Locate every Plasmodium falciparum-infected red blood cell.
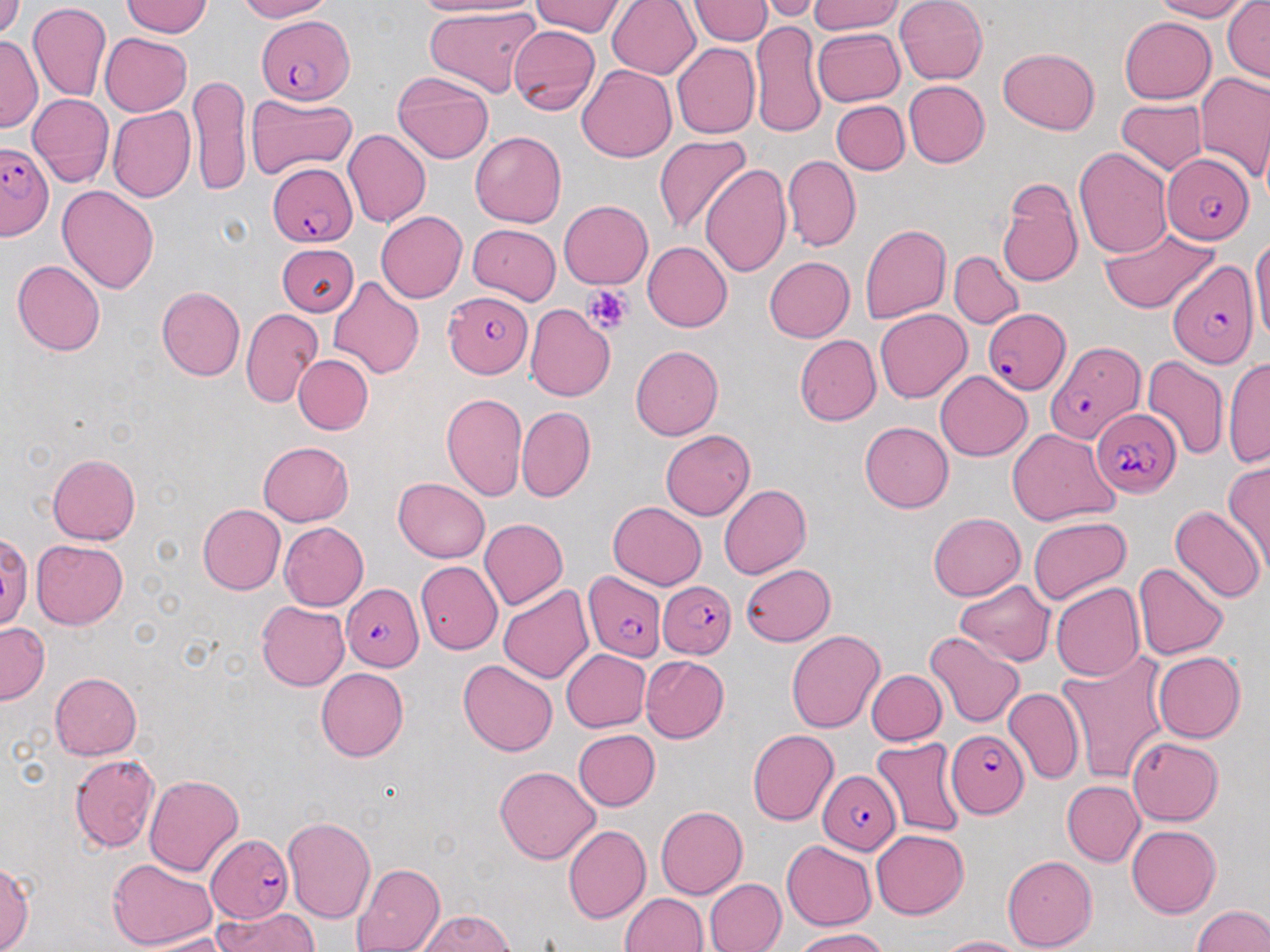

Approximate bounding boxes as named x1/y1/x2/y2 corners in pixels.
Plasmodium falciparum-infected red blood cells: (x1=258, y1=13, x2=354, y2=103), (x1=0, y1=142, x2=54, y2=241), (x1=1162, y1=152, x2=1254, y2=244), (x1=266, y1=162, x2=356, y2=247), (x1=1168, y1=257, x2=1259, y2=366), (x1=443, y1=291, x2=532, y2=377), (x1=982, y1=308, x2=1070, y2=394), (x1=1042, y1=340, x2=1145, y2=447), (x1=1091, y1=408, x2=1182, y2=497), (x1=583, y1=572, x2=666, y2=660), (x1=658, y1=582, x2=736, y2=659), (x1=339, y1=583, x2=424, y2=670), (x1=948, y1=727, x2=1029, y2=817), (x1=816, y1=770, x2=901, y2=853), (x1=206, y1=834, x2=293, y2=922).

Platelet locations: (x1=584, y1=285, x2=631, y2=333). Uninfected red blood cell locations: (x1=0, y1=0, x2=26, y2=40), (x1=236, y1=0, x2=332, y2=22), (x1=411, y1=0, x2=533, y2=18), (x1=689, y1=0, x2=774, y2=44), (x1=811, y1=0, x2=902, y2=35), (x1=894, y1=0, x2=987, y2=85), (x1=1149, y1=0, x2=1252, y2=21), (x1=1222, y1=0, x2=1269, y2=81), (x1=121, y1=1, x2=213, y2=36), (x1=529, y1=1, x2=626, y2=37), (x1=607, y1=1, x2=700, y2=79), (x1=757, y1=1, x2=825, y2=22), (x1=27, y1=3, x2=112, y2=102), (x1=422, y1=5, x2=545, y2=99), (x1=1119, y1=16, x2=1216, y2=103), (x1=749, y1=19, x2=826, y2=140), (x1=508, y1=24, x2=599, y2=113), (x1=813, y1=28, x2=904, y2=106), (x1=100, y1=32, x2=192, y2=116), (x1=0, y1=35, x2=42, y2=132), (x1=672, y1=42, x2=761, y2=139), (x1=997, y1=47, x2=1100, y2=135), (x1=578, y1=65, x2=677, y2=163), (x1=392, y1=70, x2=493, y2=163), (x1=1194, y1=70, x2=1270, y2=182), (x1=190, y1=74, x2=250, y2=195), (x1=904, y1=80, x2=990, y2=167), (x1=247, y1=92, x2=356, y2=181), (x1=27, y1=93, x2=114, y2=188), (x1=1116, y1=100, x2=1208, y2=174), (x1=831, y1=101, x2=910, y2=175), (x1=107, y1=107, x2=196, y2=203), (x1=342, y1=130, x2=431, y2=228), (x1=470, y1=131, x2=566, y2=227), (x1=654, y1=135, x2=750, y2=236), (x1=1073, y1=148, x2=1172, y2=257), (x1=782, y1=155, x2=861, y2=251), (x1=700, y1=164, x2=791, y2=277), (x1=997, y1=178, x2=1083, y2=287), (x1=57, y1=185, x2=160, y2=294), (x1=559, y1=200, x2=653, y2=289), (x1=375, y1=211, x2=468, y2=303), (x1=468, y1=224, x2=560, y2=302), (x1=859, y1=224, x2=951, y2=324), (x1=1101, y1=225, x2=1220, y2=313), (x1=1250, y1=229, x2=1270, y2=350), (x1=642, y1=241, x2=732, y2=331), (x1=278, y1=244, x2=358, y2=316), (x1=949, y1=251, x2=1023, y2=329), (x1=764, y1=256, x2=855, y2=342), (x1=13, y1=259, x2=105, y2=356), (x1=328, y1=276, x2=425, y2=378), (x1=156, y1=286, x2=245, y2=380), (x1=524, y1=304, x2=616, y2=401), (x1=241, y1=308, x2=322, y2=408), (x1=875, y1=308, x2=971, y2=403), (x1=794, y1=335, x2=881, y2=426), (x1=630, y1=345, x2=724, y2=440), (x1=294, y1=354, x2=373, y2=435), (x1=1223, y1=354, x2=1269, y2=468), (x1=1142, y1=355, x2=1229, y2=462), (x1=934, y1=369, x2=1032, y2=461), (x1=440, y1=393, x2=527, y2=501), (x1=517, y1=406, x2=596, y2=502), (x1=859, y1=421, x2=954, y2=512), (x1=1007, y1=427, x2=1119, y2=525), (x1=659, y1=429, x2=756, y2=520), (x1=257, y1=441, x2=354, y2=526), (x1=47, y1=453, x2=141, y2=544), (x1=1223, y1=461, x2=1270, y2=573), (x1=393, y1=477, x2=490, y2=563), (x1=719, y1=484, x2=811, y2=579), (x1=607, y1=502, x2=707, y2=589), (x1=197, y1=504, x2=286, y2=595), (x1=1170, y1=505, x2=1264, y2=603), (x1=928, y1=511, x2=1026, y2=600), (x1=1028, y1=517, x2=1131, y2=606), (x1=479, y1=518, x2=569, y2=610), (x1=279, y1=522, x2=369, y2=610), (x1=31, y1=539, x2=128, y2=628), (x1=416, y1=561, x2=502, y2=654), (x1=1133, y1=561, x2=1230, y2=660), (x1=740, y1=564, x2=836, y2=646), (x1=955, y1=579, x2=1054, y2=667), (x1=1051, y1=582, x2=1145, y2=682), (x1=498, y1=584, x2=594, y2=684), (x1=256, y1=601, x2=350, y2=691), (x1=0, y1=622, x2=49, y2=704), (x1=786, y1=629, x2=884, y2=732), (x1=925, y1=631, x2=1025, y2=728), (x1=561, y1=648, x2=651, y2=732), (x1=1152, y1=650, x2=1246, y2=743), (x1=640, y1=654, x2=729, y2=742), (x1=1057, y1=654, x2=1170, y2=784), (x1=458, y1=660, x2=557, y2=756), (x1=316, y1=667, x2=409, y2=761), (x1=866, y1=670, x2=946, y2=745), (x1=49, y1=672, x2=141, y2=759), (x1=1003, y1=685, x2=1084, y2=784), (x1=748, y1=729, x2=839, y2=825), (x1=572, y1=730, x2=660, y2=810), (x1=870, y1=737, x2=966, y2=837), (x1=1128, y1=737, x2=1223, y2=825), (x1=69, y1=754, x2=160, y2=853), (x1=495, y1=765, x2=600, y2=863), (x1=144, y1=774, x2=244, y2=876), (x1=1061, y1=780, x2=1144, y2=866), (x1=656, y1=806, x2=748, y2=899), (x1=282, y1=816, x2=376, y2=922), (x1=1127, y1=824, x2=1221, y2=917), (x1=563, y1=825, x2=650, y2=923), (x1=871, y1=830, x2=967, y2=919), (x1=782, y1=840, x2=876, y2=930), (x1=1003, y1=854, x2=1097, y2=950), (x1=107, y1=857, x2=218, y2=950), (x1=0, y1=862, x2=34, y2=951), (x1=351, y1=863, x2=445, y2=952), (x1=705, y1=878, x2=786, y2=952), (x1=620, y1=892, x2=707, y2=952), (x1=1192, y1=905, x2=1270, y2=952), (x1=213, y1=907, x2=318, y2=952), (x1=417, y1=910, x2=514, y2=951), (x1=792, y1=928, x2=886, y2=951), (x1=132, y1=932, x2=231, y2=951), (x1=934, y1=935, x2=1028, y2=952). Slide-level diagnosis: Plasmodium falciparum. Optical microscopy. Thin blood film. Image is 1270×952 pixels. May-Grünwald-Giemsa-stained preparation. One field of a larger specimen. 1000x magnification.